Locate every Plasmodium parasite.
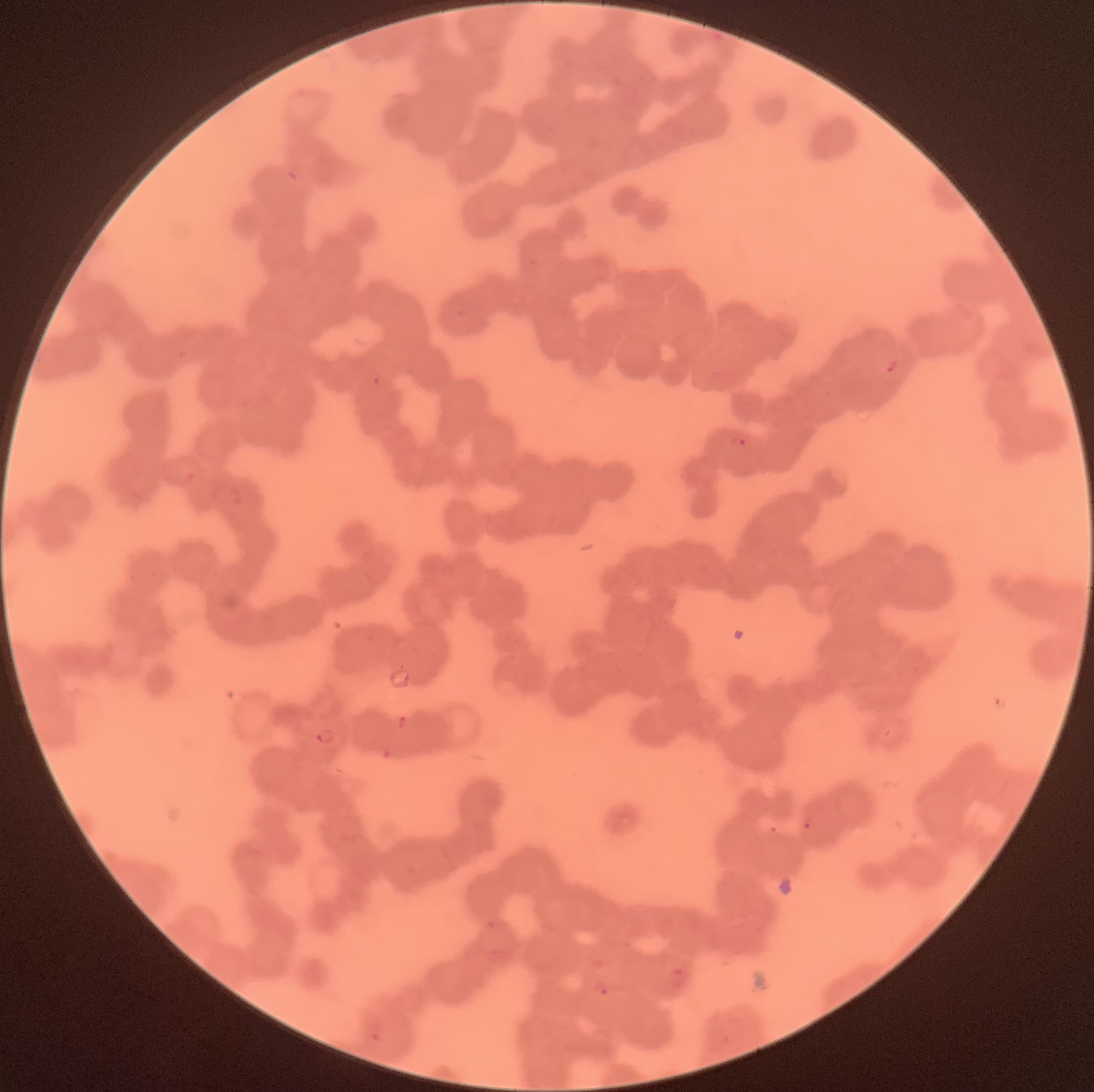
Approximate bounding boxes as [x1, y1, x2, y2] in pixels.
Plasmodium parasites: [885, 358, 904, 375], [728, 434, 748, 450], [397, 715, 410, 732], [313, 727, 338, 746], [802, 817, 818, 832], [593, 979, 614, 999].

The red blood cells show rouleaux formation. Optical microscopy. Thin blood film. Image is 1094×1092 pixels.